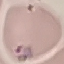

malaria status = parasitized
capture = smartphone through the microscope eyepiece
stain = Giemsa
preparation = thin smear
image type = automatically extracted cell patch, resized to 64 × 64 pixels